Identify the blood parasite species.
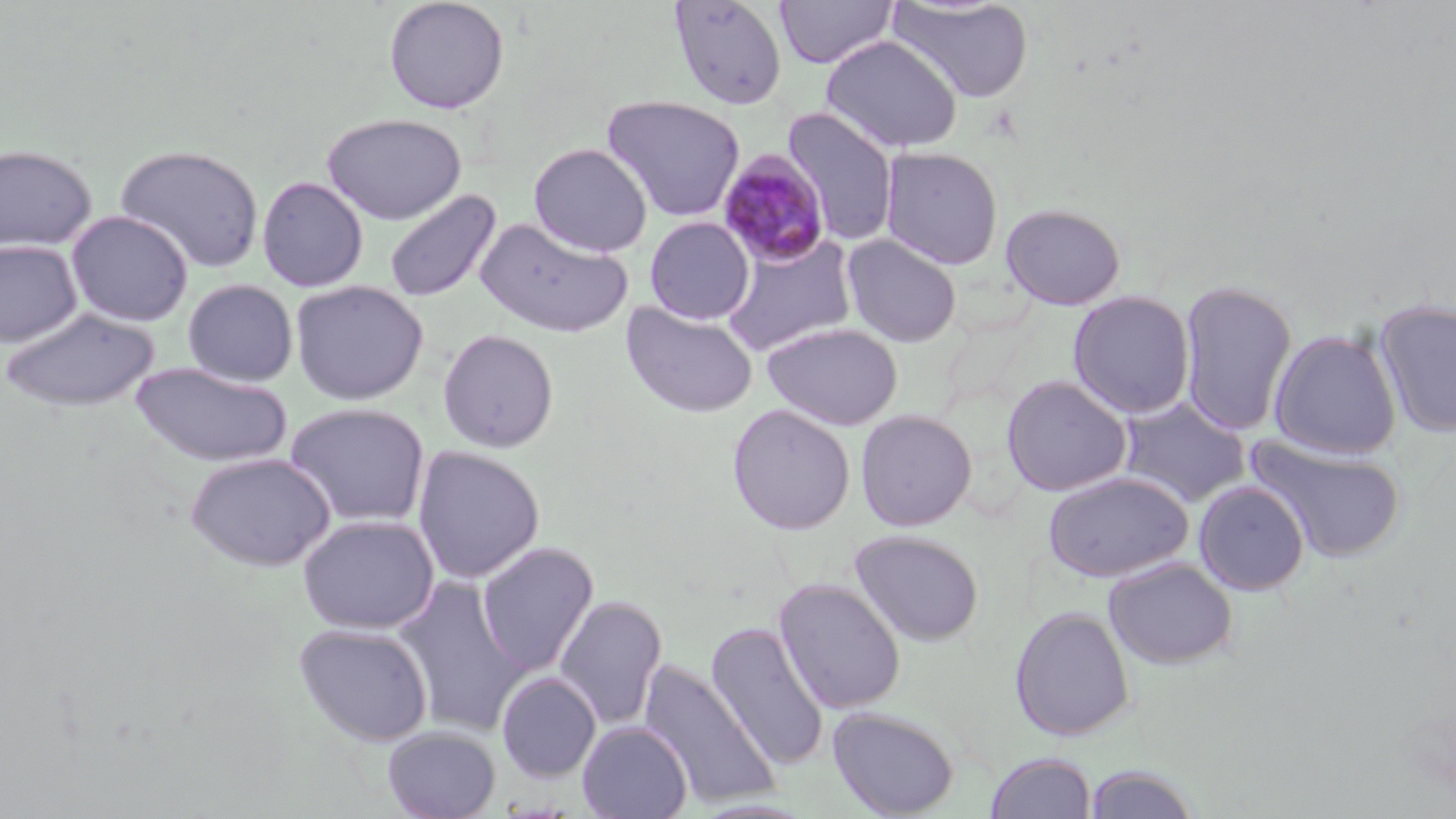

Plasmodium malariae.

Summary:
  - Coordinate format: approximate bounding boxes as [x1, y1, x2, y2] in pixels
  - Plasmodium malariae-infected red blood cell locations: [718, 150, 831, 268]
  - Uninfected red blood cell locations: [383, 0, 511, 115], [668, 0, 788, 111], [775, 0, 898, 68], [888, 0, 1034, 104], [821, 35, 963, 153], [602, 95, 746, 222], [782, 107, 900, 247], [322, 113, 467, 225], [528, 142, 653, 257], [0, 143, 98, 253], [114, 143, 265, 274], [880, 146, 1004, 270], [256, 176, 369, 292], [384, 189, 502, 303], [1000, 203, 1126, 310], [65, 210, 194, 326], [644, 216, 754, 325], [475, 217, 633, 338], [720, 233, 859, 356], [842, 234, 963, 347], [0, 239, 83, 348], [182, 279, 299, 386], [1179, 279, 1297, 438], [290, 280, 429, 405], [1067, 290, 1195, 419], [1373, 299, 1456, 438], [621, 301, 759, 418], [2, 307, 159, 413], [762, 322, 903, 431], [437, 328, 560, 454], [1268, 329, 1402, 459], [129, 361, 293, 468], [1001, 375, 1133, 497], [1116, 396, 1251, 507], [284, 402, 431, 528], [726, 403, 856, 535], [855, 409, 978, 531], [1245, 434, 1407, 564], [412, 446, 545, 583], [184, 451, 336, 572], [1042, 470, 1194, 582], [1194, 480, 1310, 596], [297, 514, 440, 634], [849, 529, 985, 647], [476, 542, 599, 676], [1104, 557, 1238, 669], [392, 576, 530, 737], [774, 577, 906, 714], [553, 593, 667, 732], [1009, 606, 1135, 741], [706, 621, 830, 772], [293, 623, 433, 746], [638, 659, 781, 811], [496, 672, 601, 783], [827, 706, 960, 818], [577, 722, 692, 819], [382, 727, 501, 819], [984, 752, 1095, 819], [1083, 764, 1201, 819]
  - Field of view: single
  - Stain: May-Grünwald-Giemsa
  - Preparation: thin blood smear
  - Image size: 1456×819 pixels
  - Modality: optical microscopy
  - Magnification: 1000x